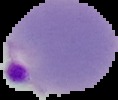

Summary:
  - Preparation: thin blood film
  - Result: malaria parasites identified
  - Image size: 118×100 pixels
  - Image type: cell region segmented out of the field of view; surrounding area masked to black